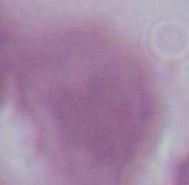
An erythrocyte is shown. 1000x magnification. Photomicrograph.